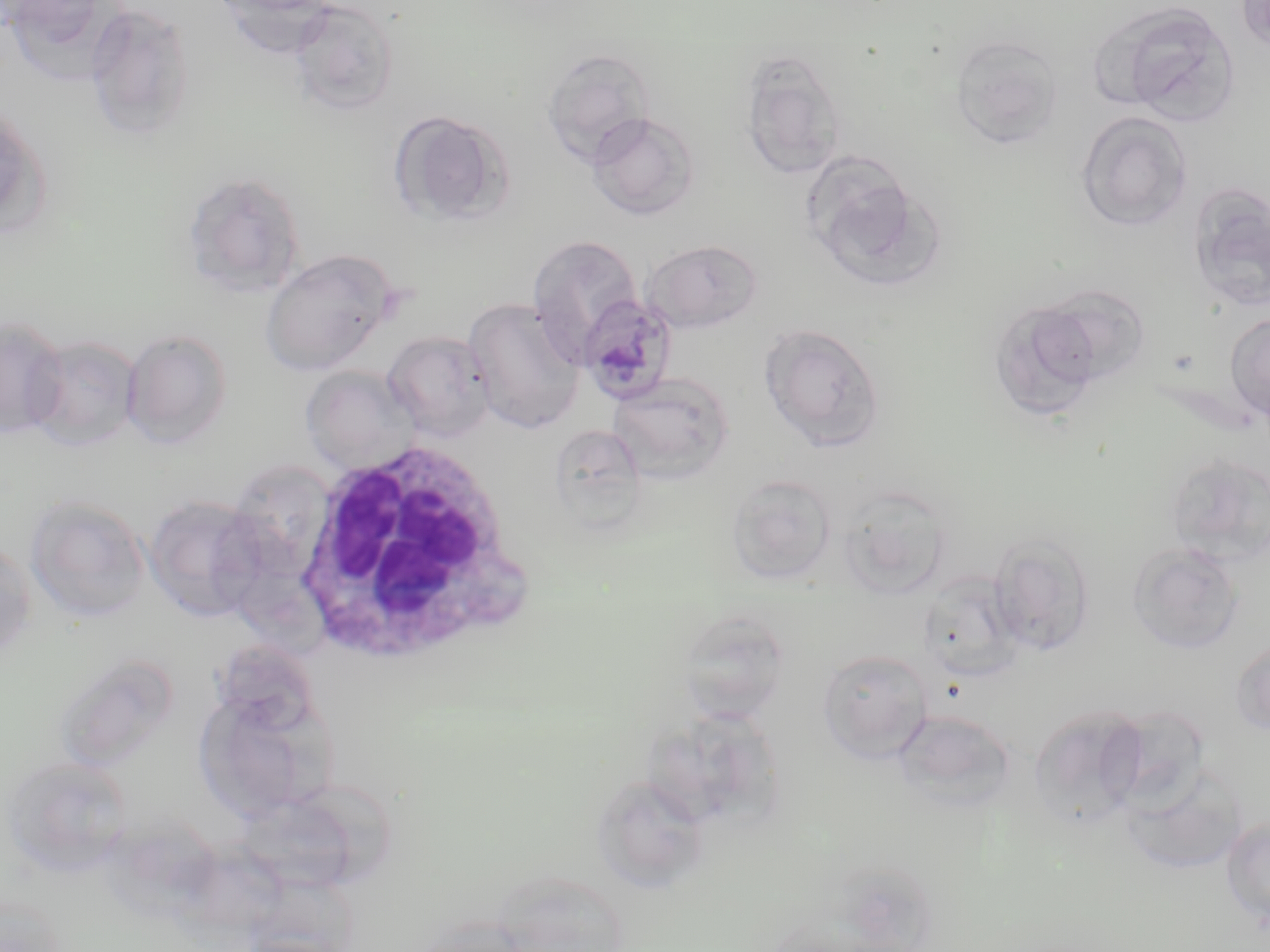
Summary:
  - Coordinate format: approximate bounding boxes as (x1, y1, x2, y2) in pixels
  - Uninfected red blood cell locations: (211, 0, 336, 55), (288, 0, 401, 116), (1094, 0, 1242, 127), (1236, 0, 1270, 52), (84, 4, 197, 141), (950, 35, 1064, 148), (540, 47, 657, 167), (738, 50, 848, 181), (0, 101, 45, 236), (388, 110, 512, 227), (1076, 111, 1193, 232), (587, 112, 700, 221), (805, 160, 938, 289), (180, 170, 306, 300), (1186, 183, 1270, 315), (526, 234, 643, 357), (641, 239, 762, 334), (260, 248, 399, 377), (1035, 283, 1152, 388), (463, 297, 586, 434), (987, 301, 1104, 422), (1225, 311, 1270, 422), (0, 315, 68, 440), (760, 323, 886, 452), (121, 329, 233, 449), (382, 330, 495, 443), (24, 335, 141, 451), (300, 365, 420, 475), (607, 372, 734, 483), (548, 425, 647, 531), (1164, 452, 1270, 566), (726, 473, 837, 585), (838, 486, 956, 599), (143, 493, 269, 624), (24, 494, 151, 624), (989, 531, 1096, 656), (0, 538, 37, 662), (1128, 541, 1243, 655), (918, 571, 1026, 684), (676, 610, 792, 724), (1231, 639, 1270, 736), (816, 649, 933, 762), (65, 663, 182, 769), (192, 689, 334, 825), (1102, 703, 1213, 814), (1029, 704, 1149, 829), (652, 708, 784, 835), (892, 709, 1016, 812), (3, 756, 134, 877), (1120, 767, 1247, 875), (591, 773, 712, 894), (306, 783, 400, 881), (245, 798, 358, 898), (1220, 815, 1270, 925), (192, 834, 295, 932), (0, 892, 68, 952)
  - Plasmodium malariae-infected red blood cell locations: (577, 292, 679, 403)
  - White blood cell locations: (295, 436, 530, 669)
  - Slide-level diagnosis: Plasmodium malariae
  - Field of view: single
  - Magnification: 1000x
  - Modality: light microscopy
  - Image size: 1270×952 pixels
  - Preparation: thin blood film
  - Stain: May-Grünwald-Giemsa